Identify the parasite.
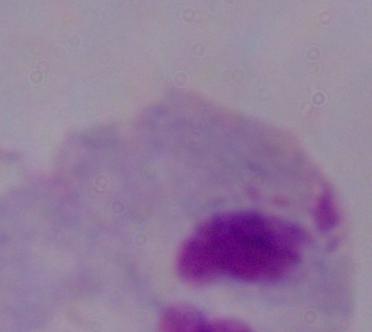
A trichomonad.

Captured at 1000x magnification. Micrograph.